Assess this cell for malaria.
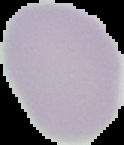

Uninfected.

Summary:
  - Image size: 124×145 pixels
  - Image type: segmented cell region on a black background
  - Preparation: thin blood smear